State which parasite is depicted.
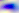

This is Toxoplasma gondii.

Summary:
  - Magnification: 400x
  - Modality: micrograph